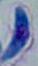

Toxoplasma gondii is seen. Captured at 1000x magnification. Micrograph.